State the preparation type.
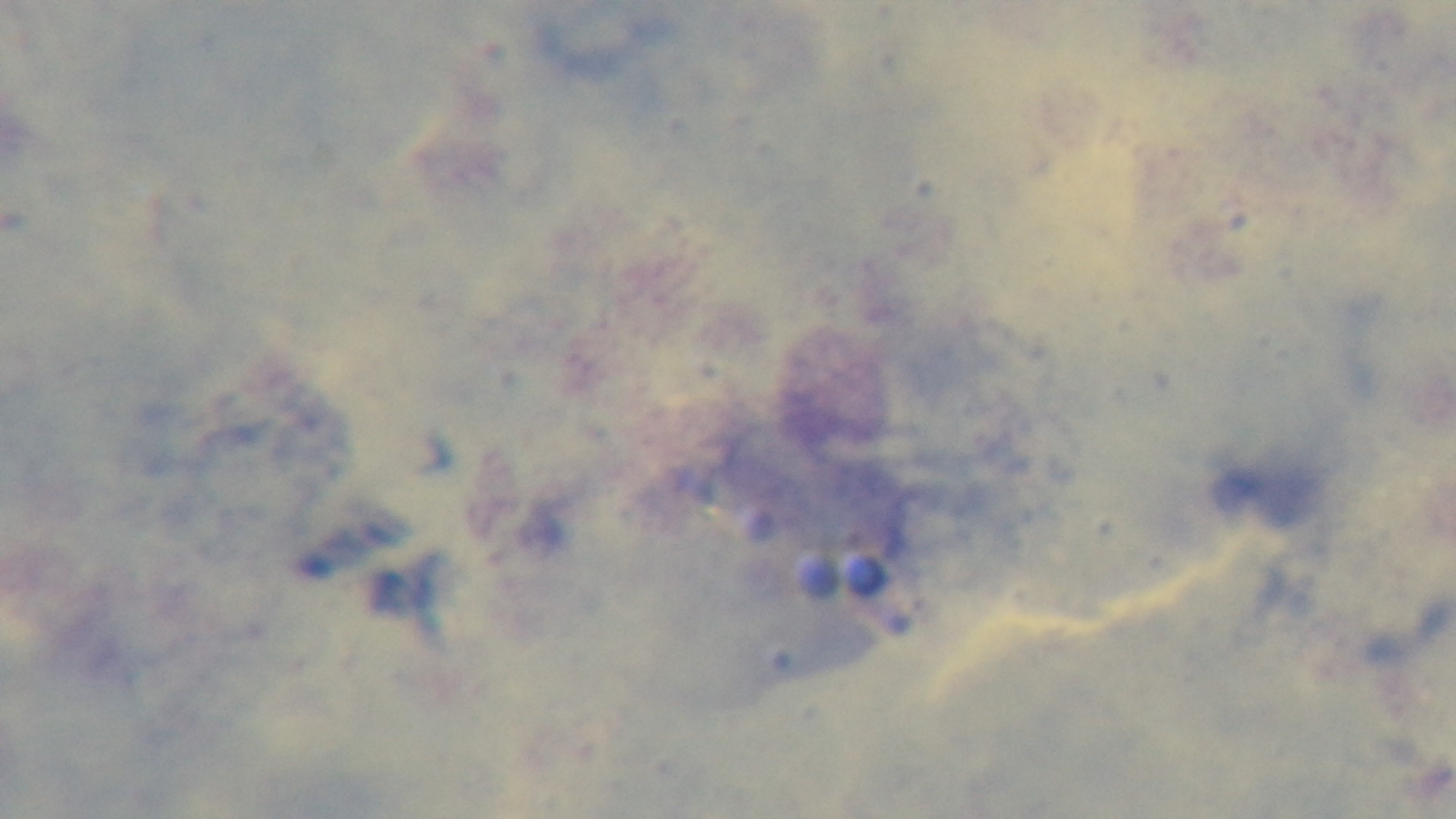

A thick smear.

Malaria status: uninfected. 100x oil-immersion objective. Light microscopy. Mounted 4K digital camera. One field from the slide. Giemsa stain.